Identify the parasite.
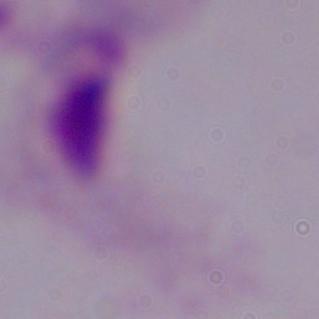
A trichomonad.

magnification = 1000x
modality = micrograph